Look for parasitized red blood cells.
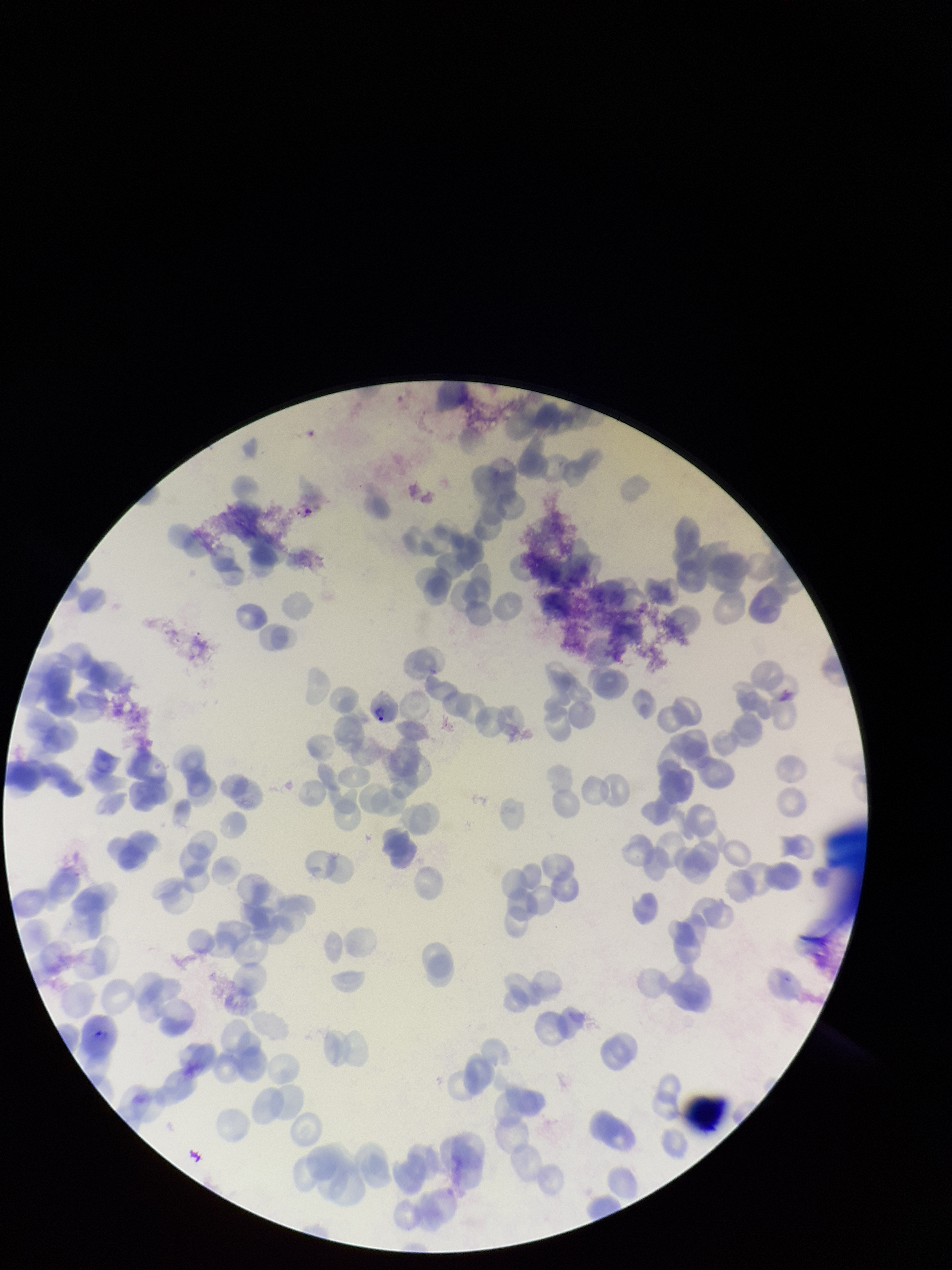

Detected.

preparation = thin
capture = smartphone photograph through the microscope eyepiece
parasitized red blood cell count = 1
patient malaria status = positive
red blood cell count = 123
stain = Giemsa
field of view = single
species reported for this patient = Plasmodium vivax
image size = 952×1270 pixels